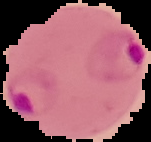
image_type: segmented cell region on a black background
image_size: 151×142 pixels
malaria_status: parasitized
preparation: thin blood smear